Classify this cell by malaria status.
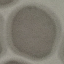
It is uninfected.

Cell patch, automatically extracted from a larger field of view and resized to 64 × 64 pixels. Giemsa-stained preparation. Photographed with a smartphone camera at the microscope eyepiece. Thin blood smear.